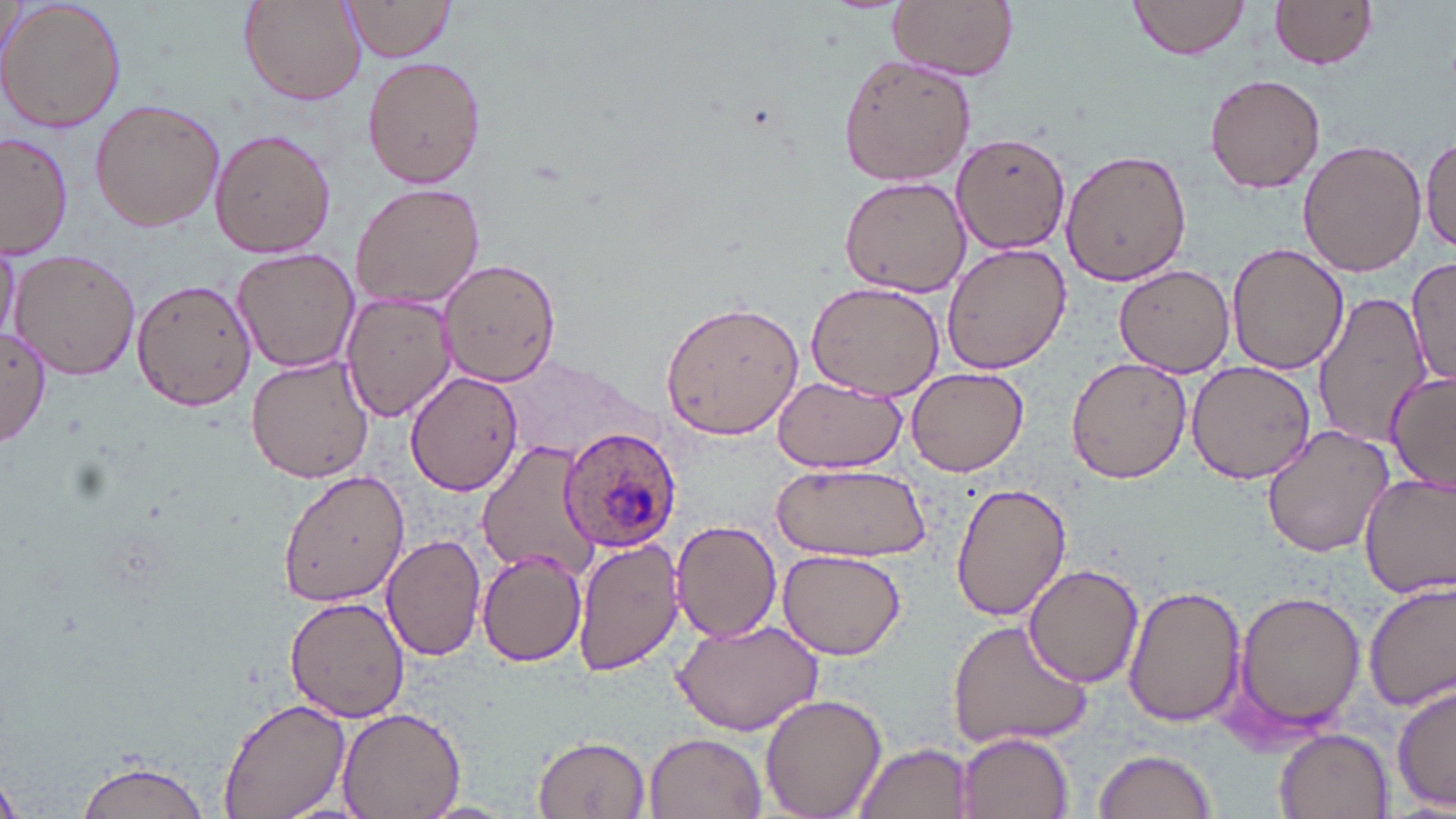
slide-level diagnosis = Plasmodium ovale
image size = 1456×819 pixels
preparation = thin blood smear
Plasmodium ovale-infected red blood cell locations = approximate bounding boxes as [x1, y1, x2, y2] in pixels: [558, 426, 681, 555]
field of view = single
magnification = 1000x
modality = light microscopy
uninfected red blood cell locations = approximate bounding boxes as [x1, y1, x2, y2] in pixels: [1, 0, 128, 135], [238, 0, 366, 106], [341, 0, 461, 62], [887, 0, 1018, 79], [1126, 0, 1251, 60], [1270, 0, 1379, 71], [836, 55, 977, 187], [362, 58, 485, 187], [1206, 70, 1327, 193], [88, 98, 226, 232], [210, 128, 336, 259], [1, 132, 74, 261], [953, 135, 1072, 254], [1420, 138, 1456, 256], [1299, 140, 1426, 278], [1060, 148, 1191, 288], [838, 177, 969, 296], [349, 180, 486, 312], [0, 235, 20, 347], [1227, 242, 1347, 375], [941, 243, 1070, 372], [231, 247, 361, 373], [9, 249, 142, 381], [1406, 257, 1456, 391], [439, 258, 559, 388], [1114, 264, 1236, 377], [132, 277, 256, 412], [805, 280, 946, 402], [341, 291, 458, 422], [1312, 294, 1427, 446], [660, 297, 807, 439], [0, 327, 52, 446], [245, 354, 375, 485], [1065, 356, 1192, 484], [1186, 360, 1316, 483], [906, 366, 1030, 477], [405, 371, 523, 495], [1384, 371, 1456, 494], [772, 378, 904, 473], [1261, 424, 1393, 557], [476, 440, 603, 578], [769, 460, 932, 564], [277, 466, 408, 608], [1359, 472, 1456, 599], [950, 482, 1072, 622], [669, 520, 781, 642], [381, 532, 485, 660], [571, 536, 684, 673], [477, 548, 588, 666], [776, 549, 906, 661], [1022, 561, 1144, 687], [1364, 579, 1456, 713], [1126, 585, 1248, 728], [1230, 588, 1364, 738], [285, 595, 411, 723], [669, 616, 823, 734], [945, 618, 1093, 751], [1392, 682, 1455, 815], [760, 693, 887, 819], [218, 697, 350, 818], [337, 706, 464, 819], [1275, 728, 1393, 818], [955, 731, 1073, 818], [644, 733, 766, 818], [533, 735, 650, 817], [854, 742, 975, 819], [1091, 747, 1218, 819], [72, 757, 215, 819], [1, 777, 24, 819]
stain = May-Grünwald-Giemsa